Identify the parasite.
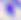

This is Toxoplasma gondii.

modality: micrograph
magnification: 400x